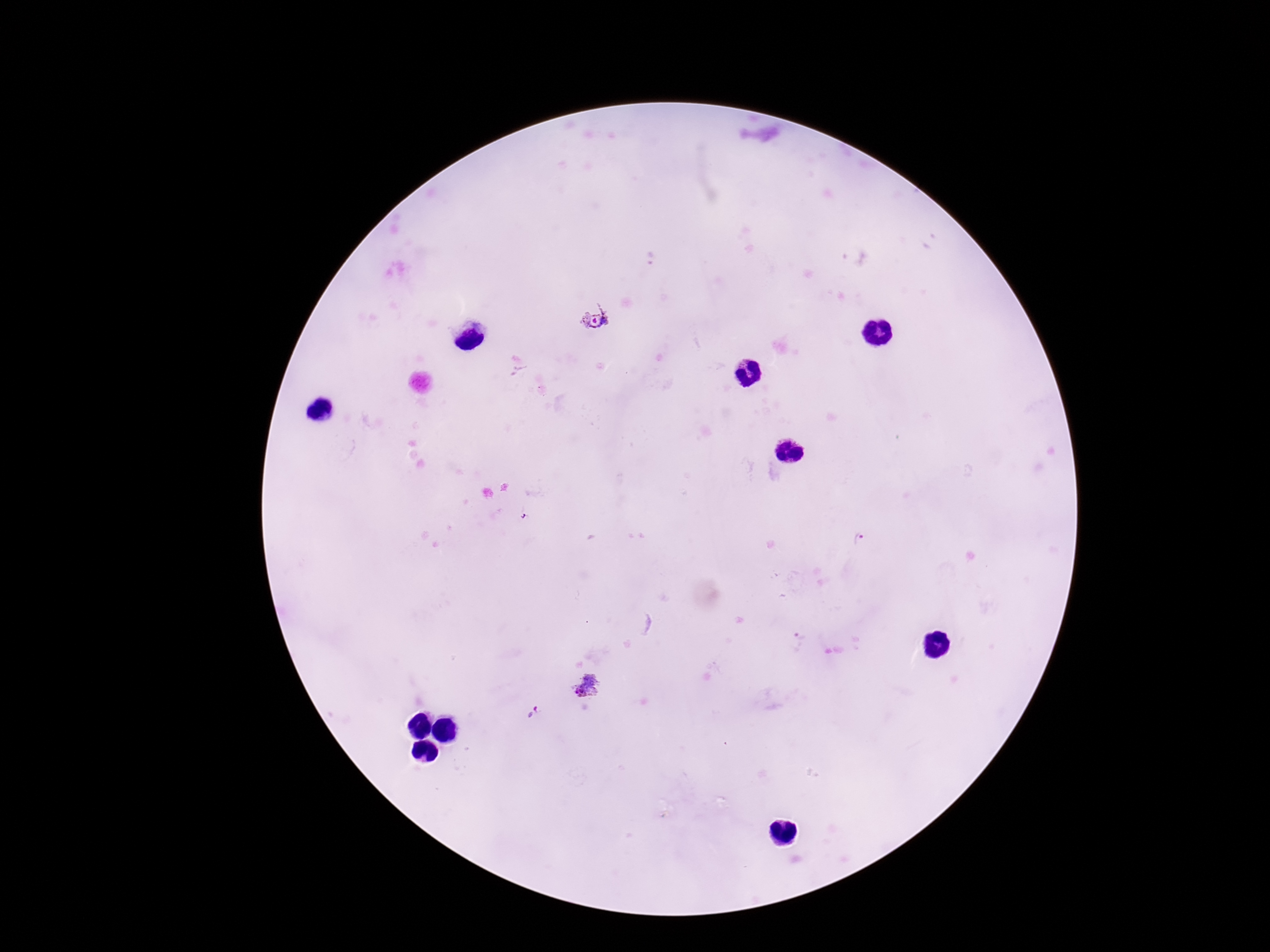
Approximate centers as (x, y) in pixels.
Summary:
  - Plasmodium parasite locations: (597, 316), (859, 540), (798, 641), (587, 685), (531, 712)
  - Stain: Giemsa
  - Magnification: 100x
  - Patient malaria status: positive
  - Preparation: thick blood film
  - Field of view: single
  - Capture: smartphone camera through the microscope eyepiece
  - Image size: 1270×952 pixels